State the preparation type.
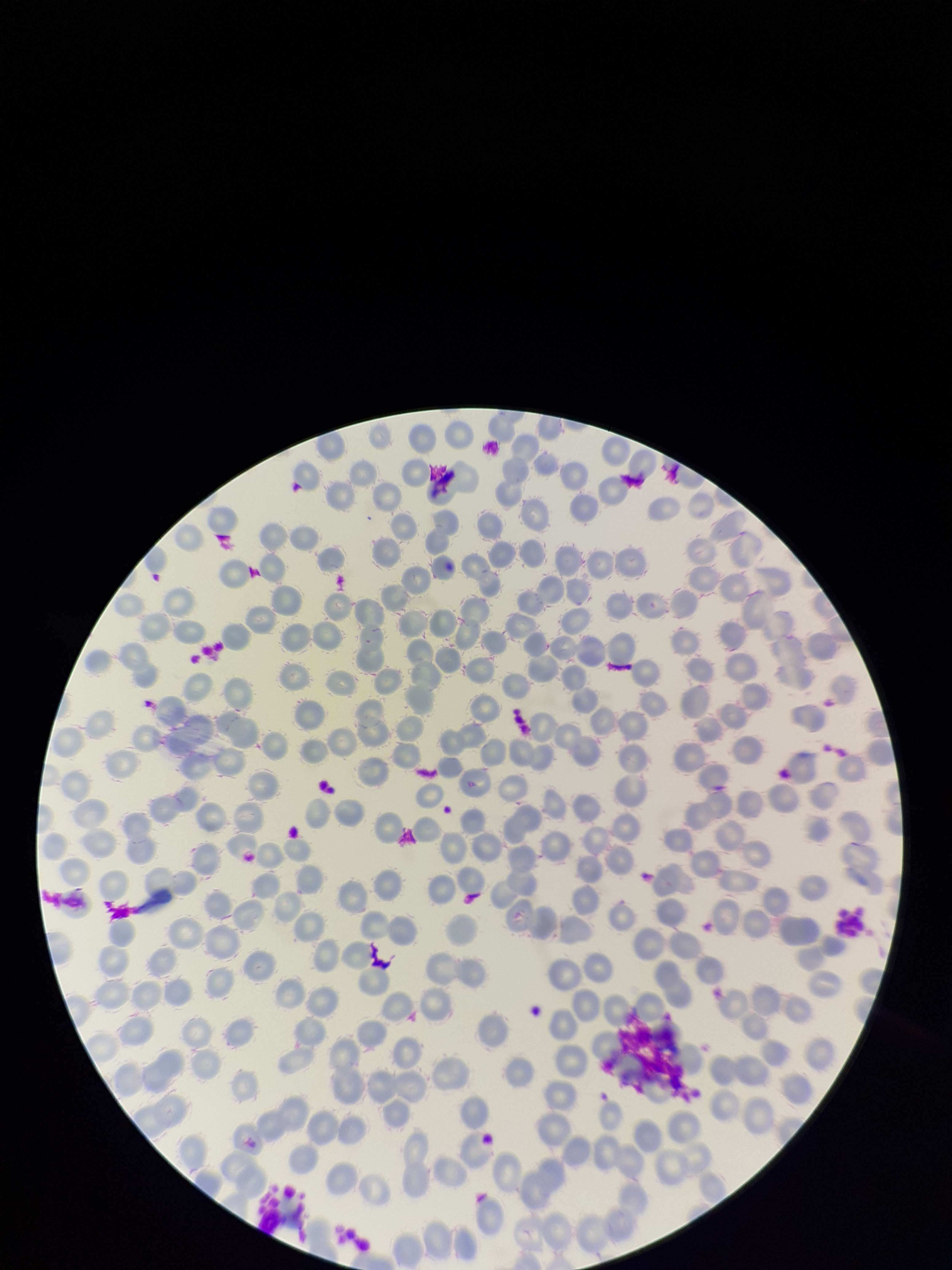

A thin smear.

Patient malaria status: negative. Red blood cell count: 223. Parasitized red blood cell count: 0. Parasitized red blood cells: none identified. One field from this slide. Photographed through the microscope eyepiece with a smartphone camera. Image is 952×1270 pixels. Stained with Giemsa.